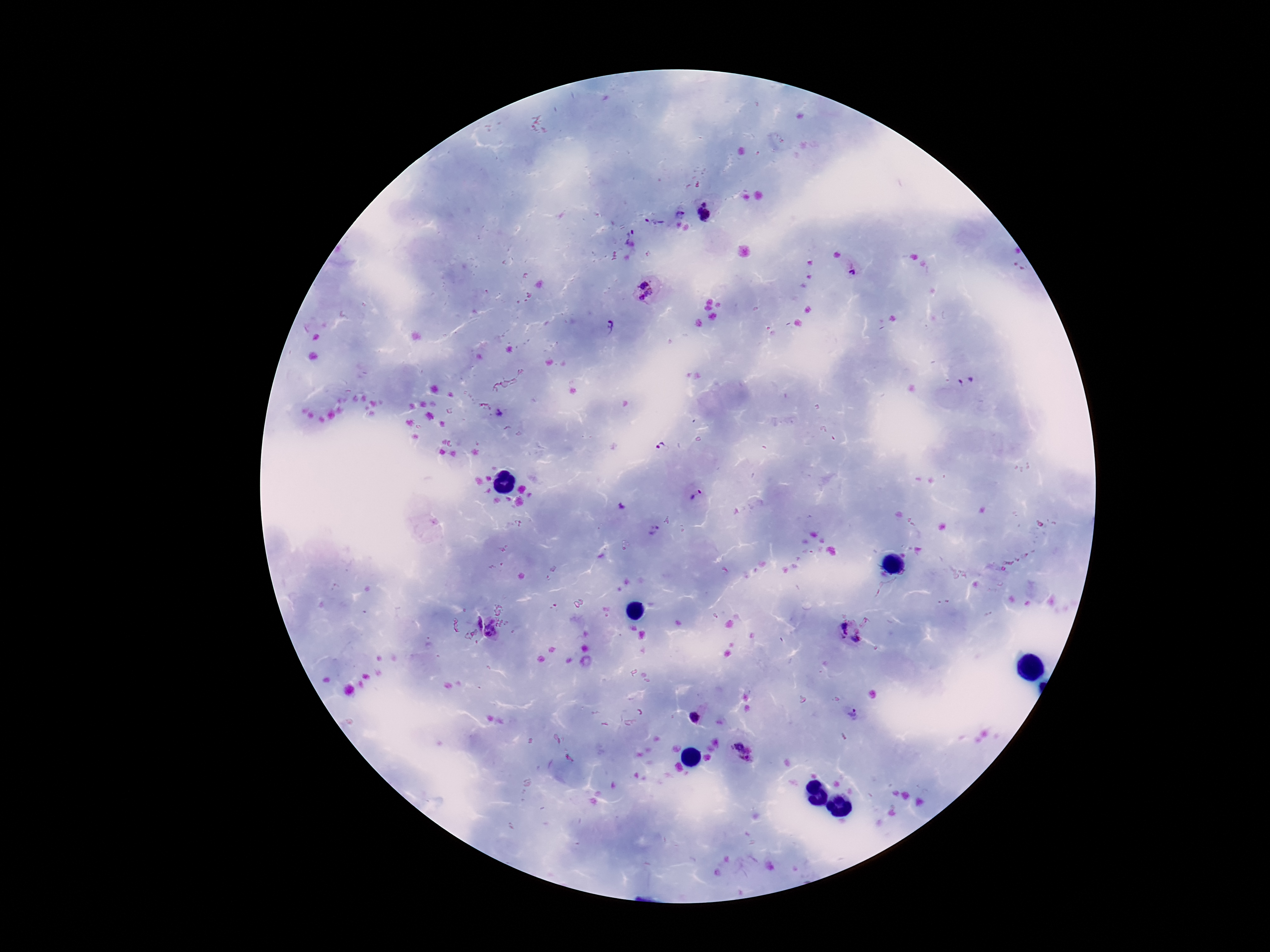
Approximate centers as (x, y) in pixels. Plasmodium parasite locations: (704, 212), (682, 213), (655, 221), (632, 237), (850, 271), (647, 290), (611, 327), (966, 381), (498, 412), (662, 449), (697, 499), (620, 506), (654, 532), (475, 622), (495, 629), (851, 631), (850, 711), (695, 718), (742, 753). 100x magnification. Image is 1270×952 pixels. Patient malaria status: positive. Single field of view. Giemsa stain. Smartphone photograph taken through the microscope eyepiece. Thick blood film.